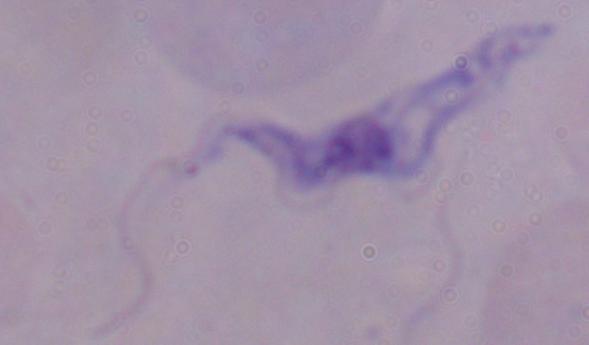

identification: trypanosome
magnification: 1000x
modality: photomicrograph